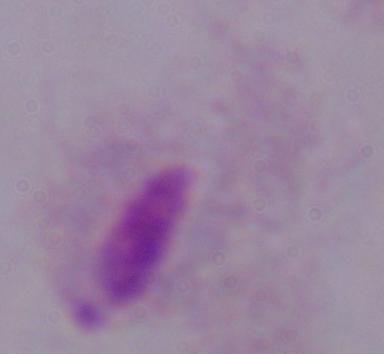
Captured at 1000x magnification. A trichomonad is seen. Micrograph.